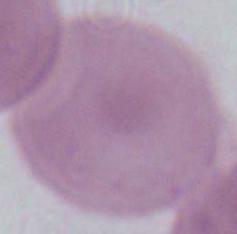

{
  "modality": "micrograph",
  "magnification": "1000x",
  "identification": "red blood cell"
}